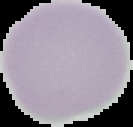

Summary:
  - Result: no Plasmodium parasites seen
  - Image type: segmented cell region with the area outside set to black
  - Image size: 133×127 pixels
  - Preparation: thin blood film